Classify this cell by malaria status.
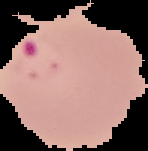
It is parasitized.

From a thin blood smear. Cell region segmented out of the field of view; the surrounding area is masked to black. Image is 148×151 pixels.